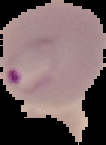
malaria status = parasitized
image type = segmented cell region on a black background
image size = 106×145 pixels
preparation = thin blood smear